Comment on the morphology of the erythrocytes.
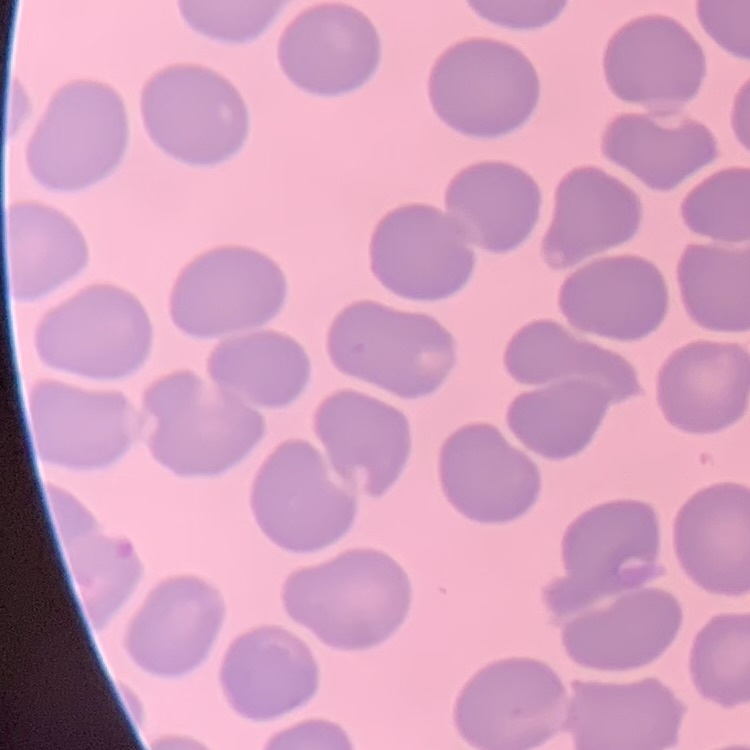
No rouleaux formation.

Summary:
  - Stain: Field's or Giemsa
  - Preparation: thin peripheral smear
  - Image type: square crop of a larger photomicrograph